Point out each leukocyte.
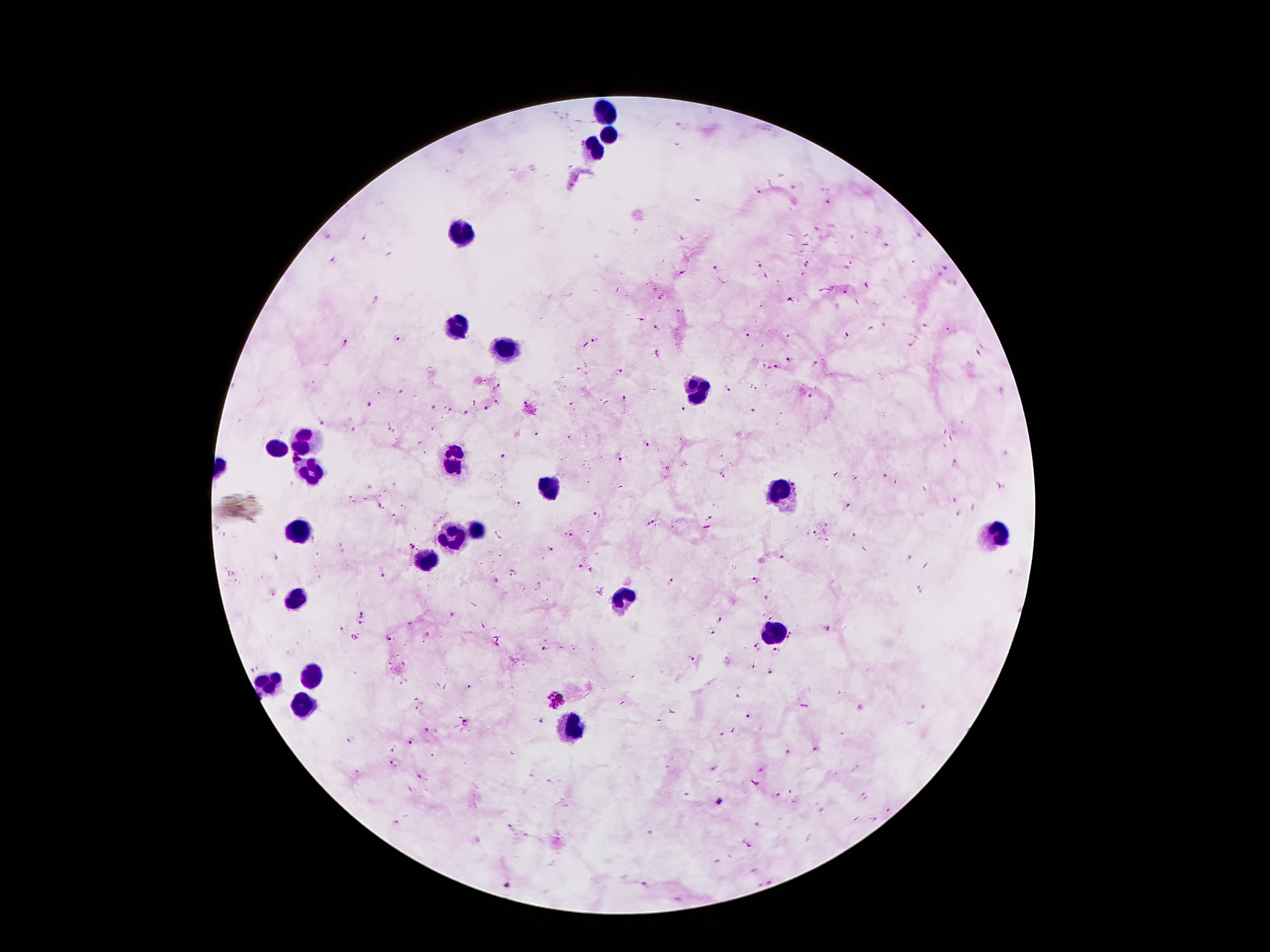
Approximate object centers, in pixels from the top-left corner.
Leukocytes: (x=610, y=112), (x=611, y=134), (x=596, y=149), (x=461, y=229), (x=460, y=328), (x=500, y=350), (x=694, y=387), (x=305, y=445), (x=274, y=449), (x=452, y=461), (x=310, y=472), (x=784, y=491), (x=551, y=492), (x=475, y=529), (x=301, y=531), (x=997, y=533), (x=454, y=541), (x=422, y=562), (x=296, y=599), (x=620, y=602), (x=770, y=635), (x=313, y=673), (x=269, y=683), (x=305, y=704), (x=571, y=725).

malaria parasite locations = (x=759, y=191), (x=828, y=203), (x=887, y=246), (x=334, y=260), (x=807, y=263), (x=758, y=264), (x=716, y=268), (x=946, y=269), (x=845, y=292), (x=790, y=302), (x=658, y=327), (x=951, y=331), (x=749, y=334), (x=845, y=336), (x=396, y=338), (x=596, y=342), (x=346, y=344), (x=788, y=359), (x=815, y=363), (x=777, y=368), (x=620, y=373), (x=499, y=387), (x=727, y=388), (x=811, y=396), (x=623, y=400), (x=497, y=402), (x=369, y=404), (x=572, y=404), (x=682, y=407), (x=433, y=408), (x=487, y=409), (x=450, y=411), (x=753, y=411), (x=467, y=414), (x=322, y=424), (x=391, y=431), (x=538, y=434), (x=647, y=444), (x=501, y=456), (x=619, y=459), (x=955, y=461), (x=722, y=475), (x=884, y=476), (x=953, y=500), (x=519, y=503), (x=380, y=506), (x=850, y=506), (x=596, y=517), (x=710, y=519), (x=650, y=524), (x=815, y=533), (x=570, y=535), (x=854, y=535), (x=410, y=546), (x=550, y=549), (x=785, y=557), (x=275, y=560), (x=579, y=566), (x=593, y=569), (x=384, y=572), (x=514, y=574), (x=755, y=580), (x=670, y=584), (x=919, y=590), (x=767, y=599), (x=362, y=615), (x=453, y=617), (x=721, y=620), (x=362, y=624), (x=409, y=626), (x=826, y=628), (x=342, y=629), (x=713, y=632), (x=428, y=636), (x=793, y=637), (x=388, y=639), (x=758, y=645), (x=545, y=649), (x=776, y=652), (x=693, y=659), (x=254, y=668), (x=770, y=673), (x=469, y=688), (x=738, y=696), (x=556, y=698), (x=749, y=716), (x=466, y=723), (x=543, y=723), (x=427, y=729), (x=723, y=734), (x=352, y=739), (x=412, y=742), (x=394, y=748), (x=815, y=750), (x=395, y=763), (x=762, y=770), (x=357, y=773), (x=418, y=777), (x=778, y=795), (x=718, y=801), (x=888, y=810), (x=397, y=824), (x=511, y=827), (x=749, y=846), (x=644, y=885)
field of view = single
stain = Giemsa
preparation = thick blood film
patient malaria status = positive for Plasmodium falciparum
magnification = 100x
image size = 1270×952 pixels
capture = smartphone camera through the microscope eyepiece